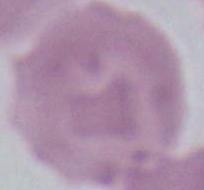

Captured at 1000x magnification. Micrograph. A red blood cell is shown.